Locate every leukocyte (white blood cell).
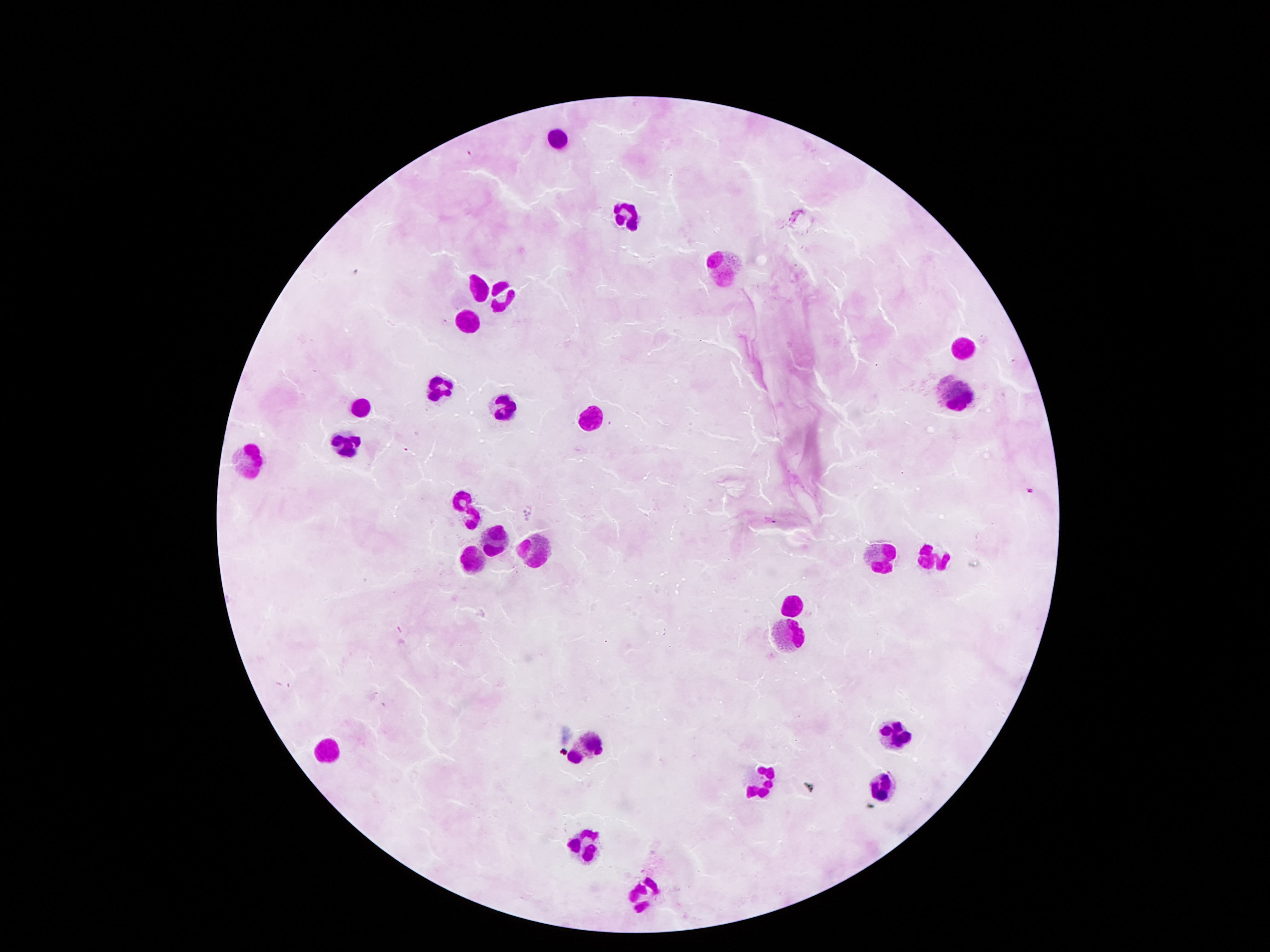

Approximate centers as {x, y} in pixels.
Leukocytes: {555, 138}, {626, 214}, {726, 272}, {476, 289}, {502, 299}, {465, 323}, {963, 350}, {443, 387}, {955, 395}, {502, 404}, {359, 406}, {590, 413}, {348, 441}, {252, 458}, {473, 509}, {496, 540}, {535, 552}, {874, 559}, {931, 559}, {468, 563}, {790, 603}, {787, 639}, {893, 734}, {590, 744}, {329, 745}, {754, 783}, {880, 785}, {580, 845}, {648, 894}.

Image is 1270×952 pixels. Photographed through the microscope eyepiece with a smartphone camera. Thick blood smear. Single field of view. Giemsa-stained preparation. 100x magnification. Patient malaria status: not infected.